Report the malaria status of this cell.
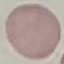
Uninfected.

Acquired by smartphone through the microscope eyepiece. Giemsa stain. Automatically extracted cell patch, resized to 64 × 64 pixels. Thin blood film.